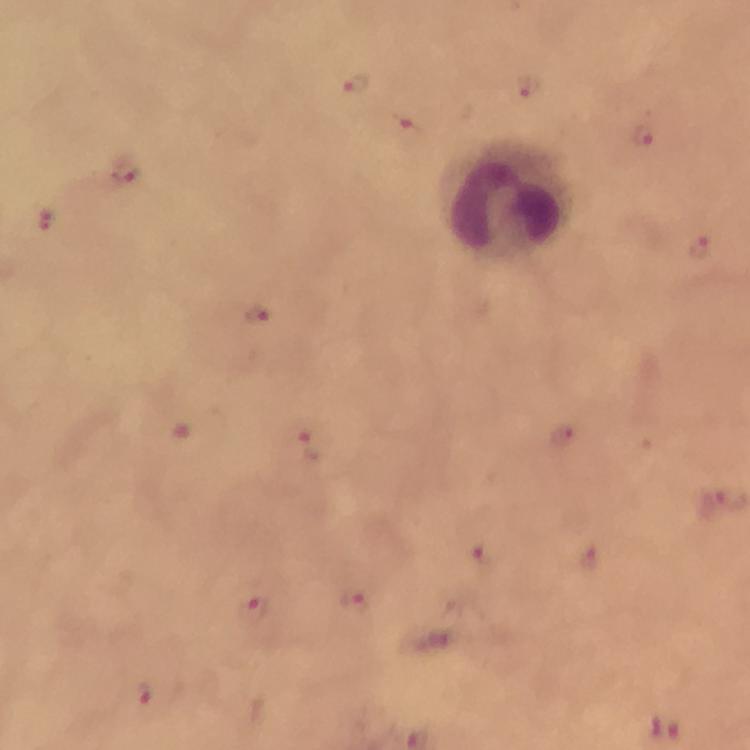
Approximate centers as (x, y) in pixels. Malaria parasite locations: (526, 84), (358, 85), (407, 132), (645, 134), (126, 169), (46, 224), (698, 246), (258, 311), (565, 437), (312, 447), (482, 559), (593, 562), (356, 601), (257, 610), (144, 697). Leukocyte locations: (506, 199). Immersion oil was used. From a diagnostic examination for malaria. Thick blood smear. Giemsa stain. Photographed through the microscope with a smartphone camera. A crop from one field of view. At 100x magnification. Image is 750×750 pixels.